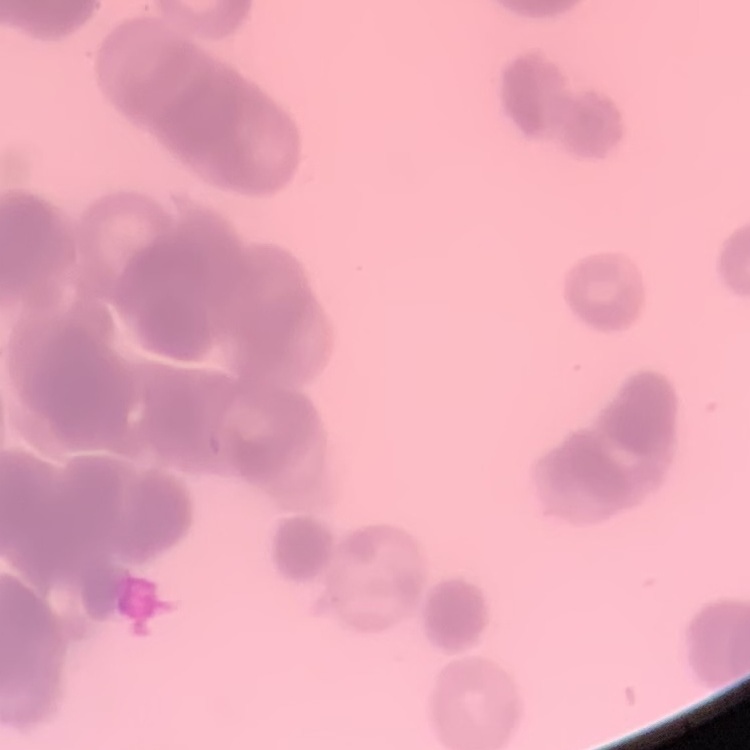

erythrocyte morphology = rouleaux formation
preparation = thin blood smear
stain = Field's or Giemsa
image type = one tile cut from a larger photomicrograph